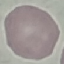
Summary:
  - Malaria status: uninfected
  - Image type: cell patch, automatically extracted from a larger field of view and resized to 64 × 64 pixels
  - Stain: Giemsa
  - Preparation: thin smear
  - Capture: smartphone through the microscope eyepiece